Identify the blood parasite species.
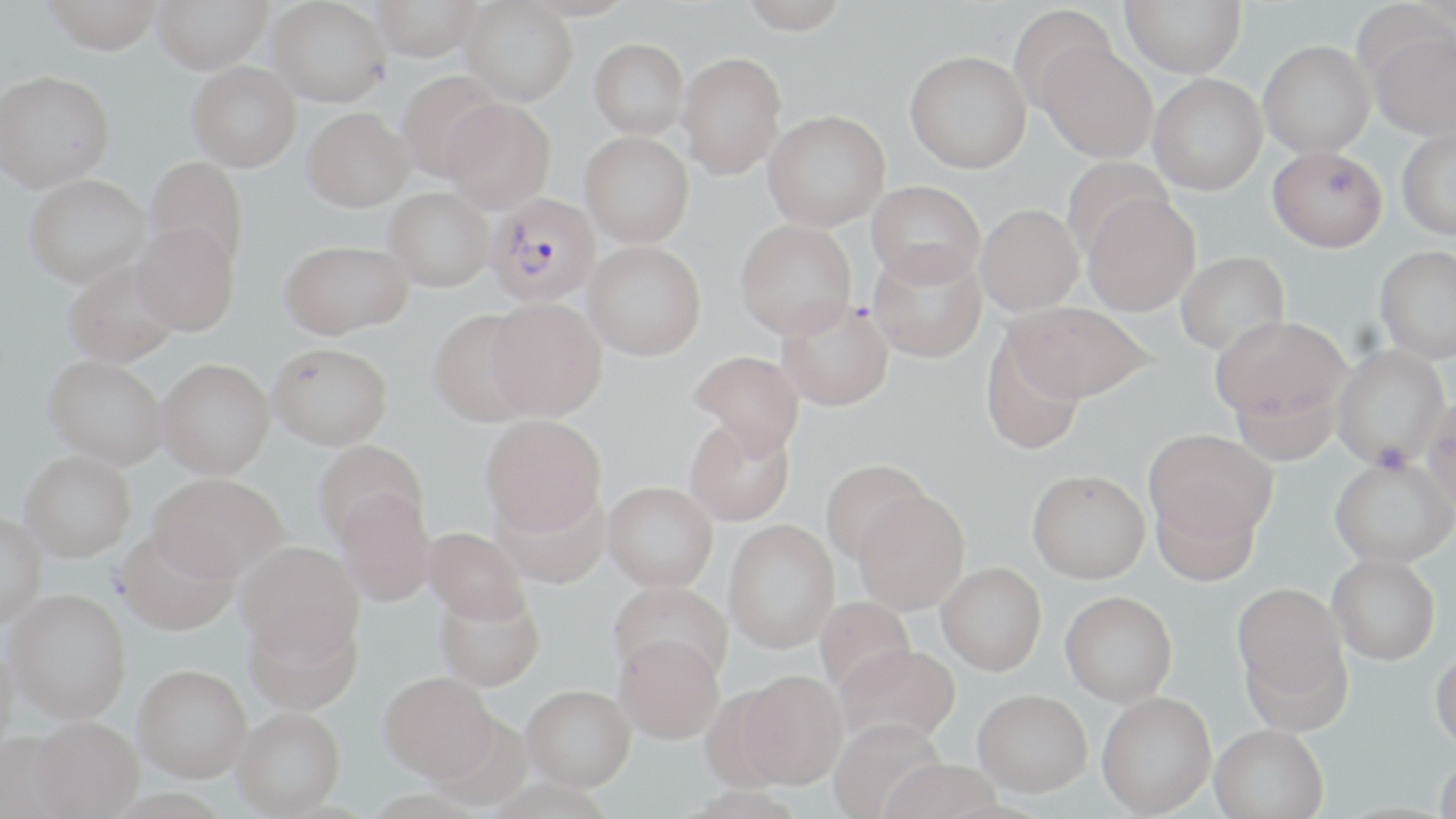

Plasmodium falciparum.

Approximate bounding boxes as (x1, y1, x2, y2) in pixels. Uninfected red blood cell locations: (43, 0, 163, 54), (152, 0, 272, 73), (267, 0, 391, 106), (370, 0, 482, 61), (516, 0, 637, 21), (739, 0, 849, 34), (1120, 0, 1246, 77), (460, 1, 577, 106), (1007, 5, 1118, 115), (1367, 29, 1456, 139), (589, 38, 689, 138), (1258, 40, 1375, 158), (1038, 42, 1158, 163), (905, 51, 1031, 173), (677, 52, 787, 179), (187, 61, 301, 171), (0, 70, 115, 192), (397, 72, 507, 182), (1148, 73, 1267, 195), (441, 98, 556, 212), (302, 108, 413, 211), (762, 109, 890, 231), (1396, 128, 1456, 239), (579, 130, 694, 247), (1268, 145, 1387, 251), (144, 155, 249, 273), (1061, 157, 1173, 259), (24, 174, 151, 287), (867, 180, 985, 287), (383, 187, 494, 292), (1082, 194, 1200, 316), (975, 203, 1084, 315), (735, 219, 856, 339), (131, 222, 239, 336), (280, 240, 413, 338), (583, 240, 706, 360), (868, 246, 987, 362), (1374, 246, 1456, 363), (1175, 251, 1289, 355), (63, 259, 183, 367), (486, 298, 606, 421), (775, 299, 893, 410), (1010, 302, 1155, 404), (428, 308, 539, 427), (1212, 317, 1350, 426), (979, 331, 1087, 457), (268, 342, 393, 450), (1331, 345, 1450, 471), (689, 350, 805, 459), (43, 354, 168, 469), (155, 358, 275, 479), (1228, 376, 1341, 467), (1422, 397, 1456, 520), (480, 414, 606, 536), (684, 420, 795, 527), (1145, 430, 1276, 550), (313, 441, 428, 548), (19, 450, 136, 562), (1329, 459, 1456, 571), (820, 460, 931, 567), (149, 472, 286, 582), (1026, 473, 1150, 588), (601, 484, 718, 595), (492, 488, 611, 591), (1150, 488, 1261, 589), (335, 490, 435, 607), (852, 492, 970, 617), (0, 514, 46, 630), (723, 521, 839, 656), (115, 528, 238, 636), (423, 528, 530, 627), (236, 541, 364, 664), (1327, 557, 1440, 668), (936, 566, 1046, 679), (609, 583, 732, 689), (1232, 586, 1348, 707), (433, 589, 545, 693), (5, 590, 131, 725), (1059, 595, 1177, 709), (813, 596, 917, 701), (243, 611, 363, 717), (613, 639, 724, 748), (0, 643, 19, 766), (834, 648, 960, 750), (1429, 651, 1456, 757), (133, 669, 251, 788), (733, 674, 848, 793), (378, 675, 498, 789), (521, 690, 636, 796), (973, 694, 1092, 802), (1096, 695, 1216, 818), (232, 711, 346, 819), (828, 720, 947, 819), (28, 722, 142, 818), (1208, 728, 1328, 819), (0, 734, 73, 819), (1434, 758, 1456, 819), (878, 763, 1003, 819), (484, 782, 612, 818), (682, 789, 804, 819), (104, 792, 233, 819), (357, 793, 488, 819). Plasmodium falciparum-infected red blood cell locations: (484, 193, 601, 307). Thin blood smear. Image is 1456×819 pixels. Light microscopy. 1000x magnification. May-Grünwald-Giemsa stain. Single field of view.